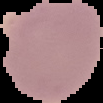

Malaria status: parasitized. From a thin blood film. The area outside the segmented cell region is set to black. Image is 103×103 pixels.